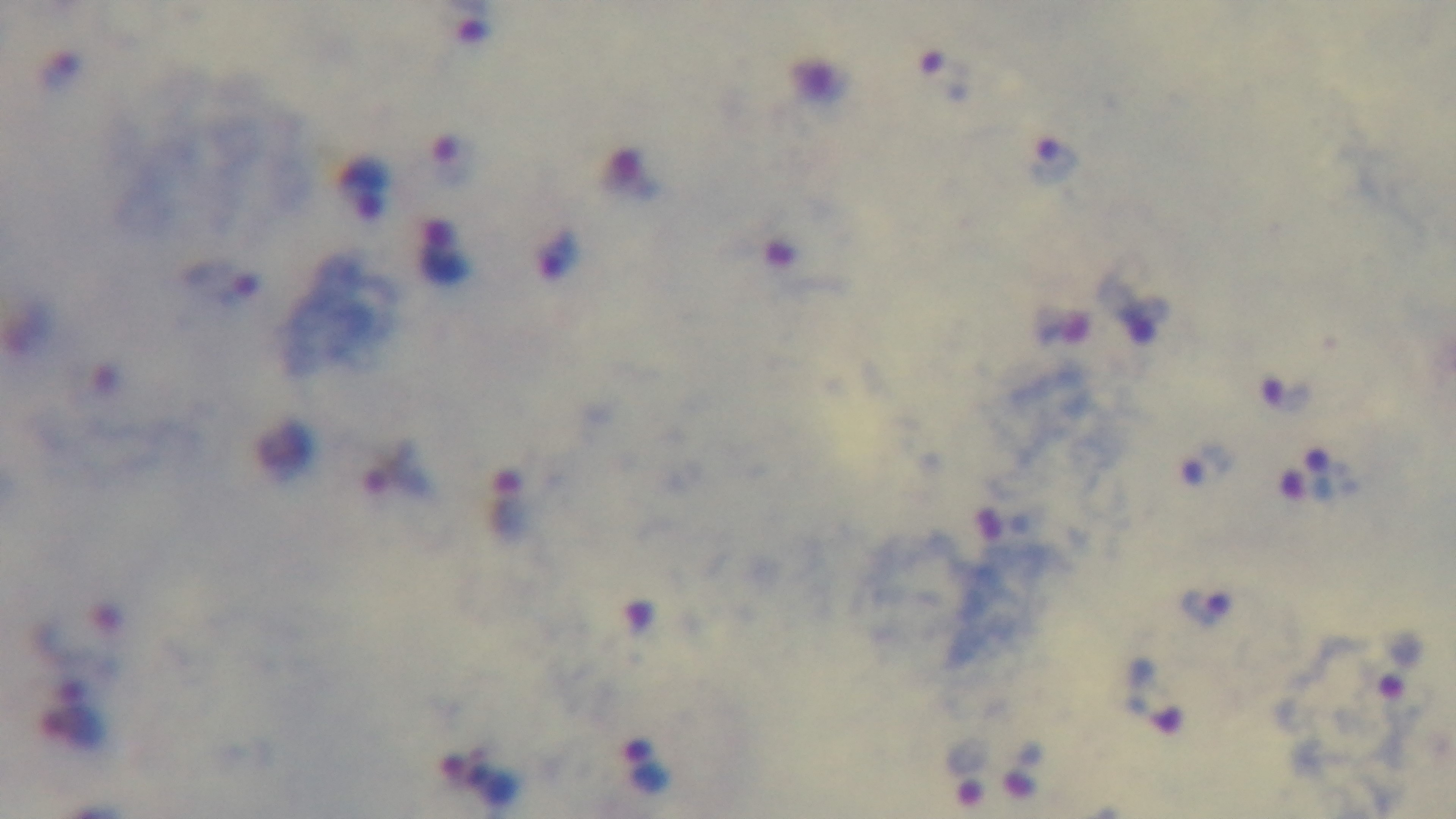
Malaria status: positive. Mounted 4K digital camera. Giemsa-stained. 100x oil-immersion objective. Light microscopy. Single field of view. Preparation: thick.